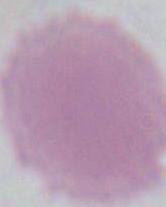

modality = photomicrograph
identification = red blood cell
magnification = 1000x